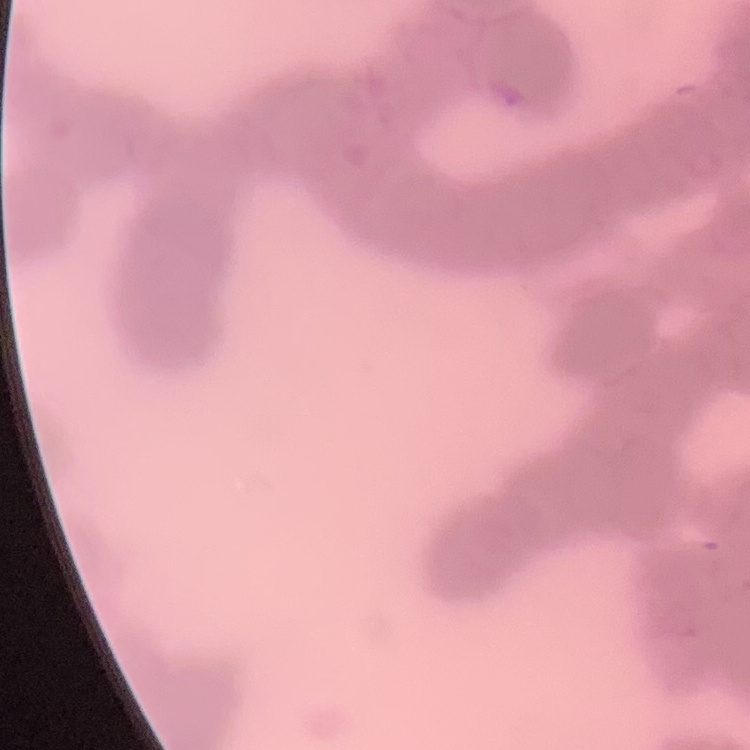

erythrocyte morphology = rouleaux formation
image type = one tile cut from a larger photomicrograph
stain = Field's or Giemsa
preparation = thin blood smear